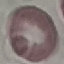
Result: no malaria parasites detected. Acquired by smartphone through the microscope eyepiece. Giemsa stain. Automatically extracted cell patch, resized to 64 × 64 pixels. Thin smear of blood.